Identify the blood parasite species.
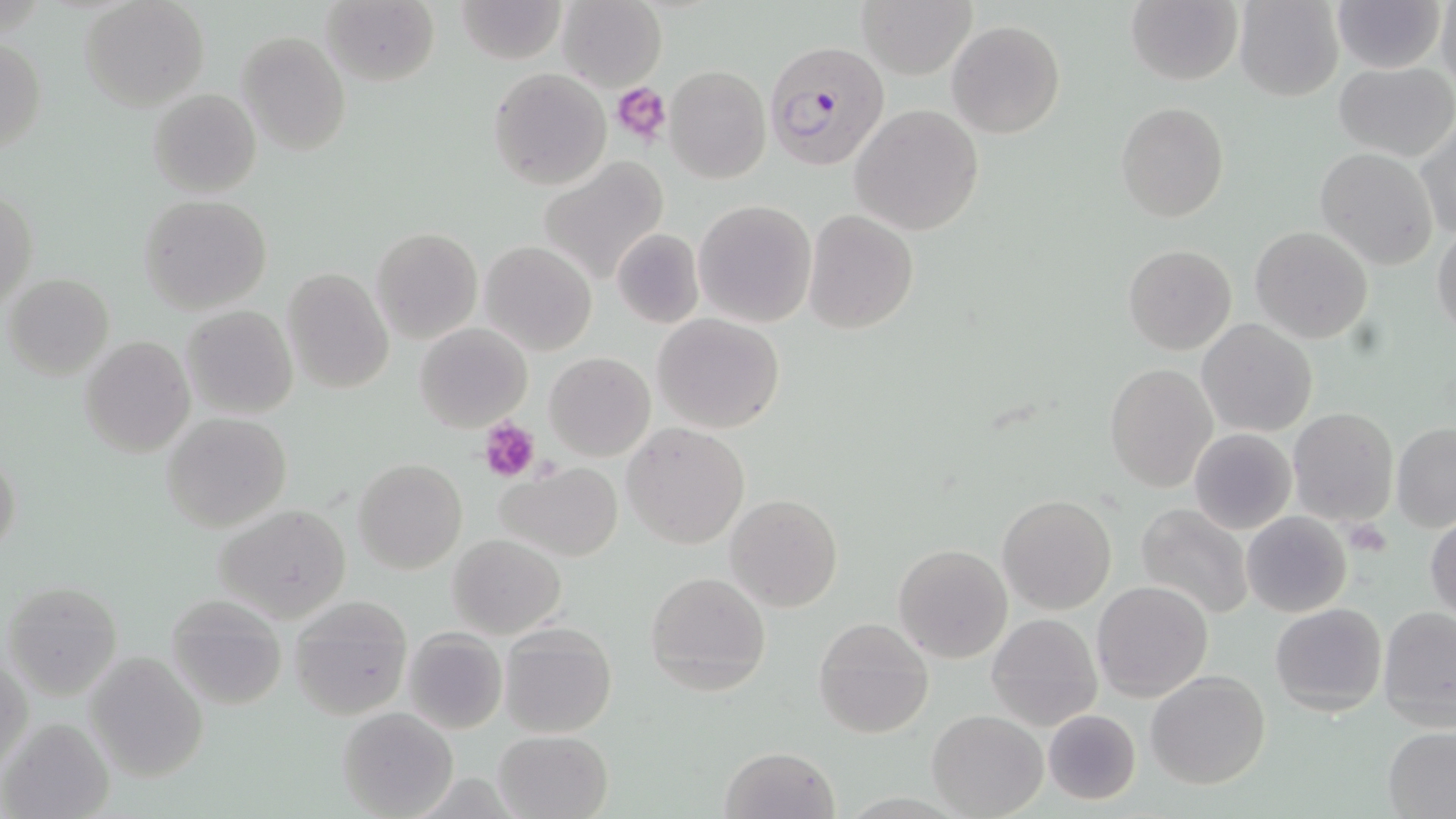

Plasmodium falciparum.

modality = optical microscopy
Plasmodium falciparum-infected red blood cell locations = approximate bounding boxes as (x1, y1, x2, y2) in pixels: (761, 40, 890, 171)
image size = 1456×819 pixels
magnification = 1000x
stain = May-Grünwald-Giemsa
platelet locations = approximate bounding boxes as (x1, y1, x2, y2) in pixels: (612, 82, 673, 146), (479, 418, 540, 481), (1343, 519, 1391, 557)
preparation = thin blood smear
uninfected red blood cell locations = approximate bounding boxes as (x1, y1, x2, y2) in pixels: (80, 0, 208, 112), (456, 0, 568, 64), (556, 0, 668, 92), (859, 0, 975, 79), (1232, 0, 1344, 101), (1334, 0, 1445, 73), (1438, 0, 1456, 95), (321, 1, 440, 87), (1125, 1, 1242, 86), (947, 19, 1066, 138), (235, 30, 351, 155), (0, 35, 45, 157), (1334, 62, 1455, 159), (664, 65, 769, 182), (488, 67, 612, 191), (148, 88, 261, 199), (1115, 102, 1229, 222), (850, 105, 984, 235), (1416, 125, 1455, 241), (1315, 147, 1439, 272), (539, 157, 671, 286), (1, 188, 36, 312), (138, 194, 271, 314), (694, 199, 818, 327), (804, 209, 919, 333), (1431, 224, 1456, 338), (1250, 226, 1373, 344), (371, 228, 483, 345), (611, 229, 704, 327), (479, 239, 597, 356), (1123, 245, 1236, 354), (282, 267, 394, 393), (3, 273, 115, 381), (180, 305, 299, 420), (652, 312, 785, 434), (1198, 319, 1317, 437), (415, 322, 533, 433), (81, 336, 194, 457), (544, 352, 655, 461), (1103, 364, 1218, 493), (1288, 408, 1398, 528), (162, 412, 292, 531), (620, 422, 751, 549), (1390, 422, 1456, 532), (1189, 427, 1297, 535), (1, 446, 23, 564), (354, 457, 467, 574), (496, 462, 622, 562), (997, 493, 1117, 615), (724, 494, 844, 612), (1135, 503, 1254, 621), (214, 504, 352, 624), (1241, 511, 1352, 619), (1424, 513, 1456, 623), (447, 534, 566, 639), (892, 544, 1013, 663), (645, 571, 771, 696), (3, 580, 122, 698), (1091, 580, 1213, 702), (167, 593, 289, 711), (288, 596, 414, 721), (1270, 602, 1387, 716), (1378, 606, 1456, 732), (987, 613, 1102, 730), (813, 616, 934, 739), (500, 622, 617, 739), (403, 629, 508, 735), (1, 650, 32, 777), (83, 651, 209, 782), (1145, 670, 1272, 789), (337, 706, 458, 819), (1042, 709, 1141, 805), (927, 710, 1047, 819), (1, 716, 114, 819), (1382, 726, 1456, 817), (494, 730, 615, 819), (719, 746, 839, 819)
field of view = one of a larger specimen